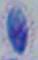

{
  "identification": "Toxoplasma gondii",
  "magnification": "1000x",
  "modality": "photomicrograph"
}